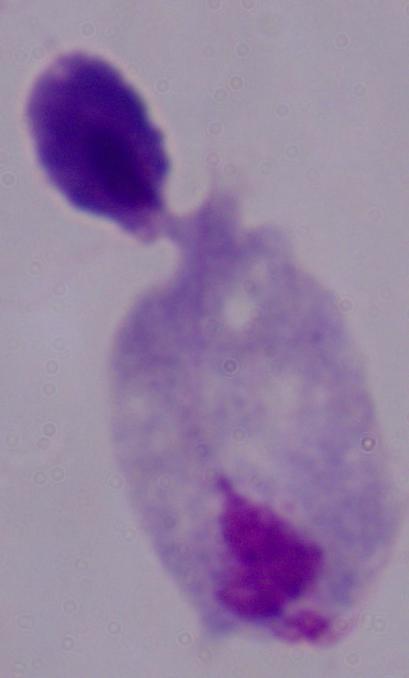

Captured at 1000x magnification. A trichomonad is shown. Photomicrograph.